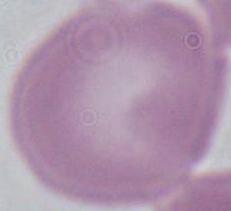

Summary:
  - Magnification: 1000x
  - Identification: red blood cell
  - Modality: photomicrograph